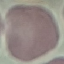

result = no malaria parasites detected
preparation = thin smear
stain = Giemsa
image type = automatically extracted cell patch, resized to 64 × 64 pixels
capture = smartphone camera at the microscope eyepiece